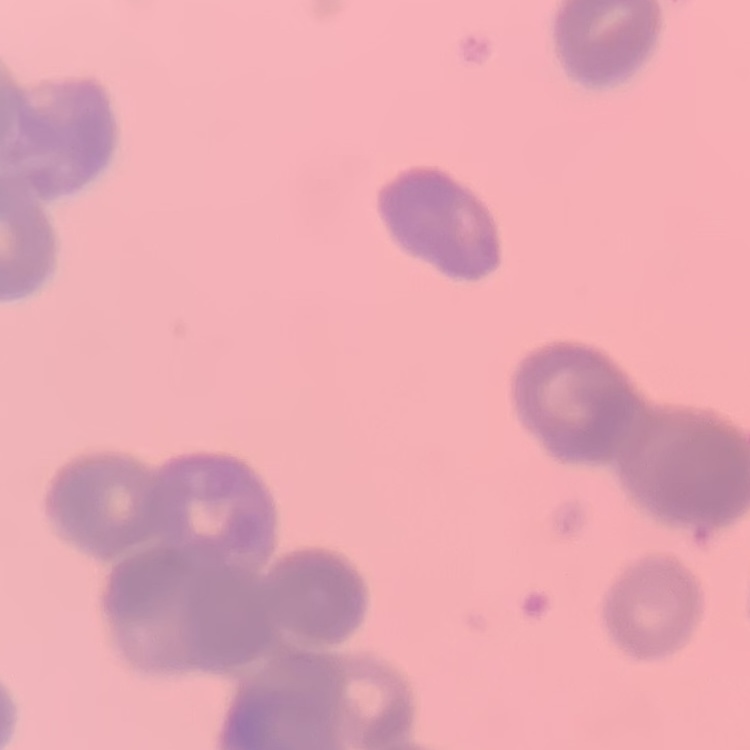
{
  "erythrocyte_morphology": "rouleaux formation",
  "stain": "Field's or Giemsa",
  "image_type": "one tile cut from a larger photomicrograph",
  "preparation": "thin peripheral smear"
}